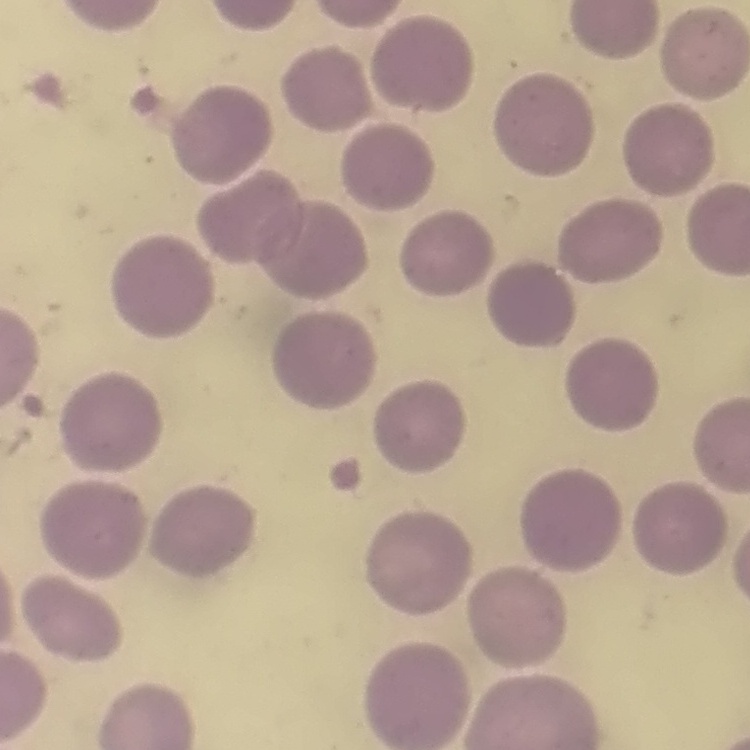
red_blood_cell_morphology: no rouleaux formation
image_type: square crop of a larger photomicrograph
preparation: thin blood film
stain: Field's or Giemsa